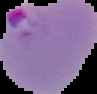

From a thin blood film. Image is 97×94 pixels. Cell region segmented out of the field of view; the surrounding area is masked to black. Malaria status: parasitized.